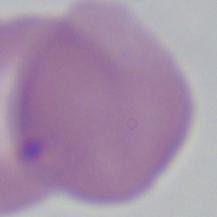
Summary:
  - Magnification: 1000x
  - Identification: Babesia
  - Modality: micrograph